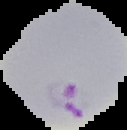

image_type: segmented cell region on a black background
result: malaria parasites detected
image_size: 127×130 pixels
preparation: thin blood film